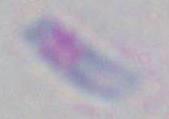 Captured at 1000x magnification. Toxoplasma gondii is shown. Micrograph.